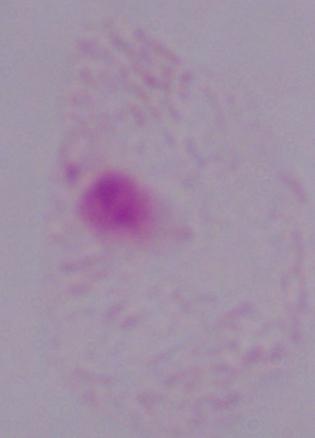
Micrograph. A trichomonad is seen. 1000x magnification.